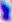
Photomicrograph. 400x magnification. Toxoplasma gondii is seen.